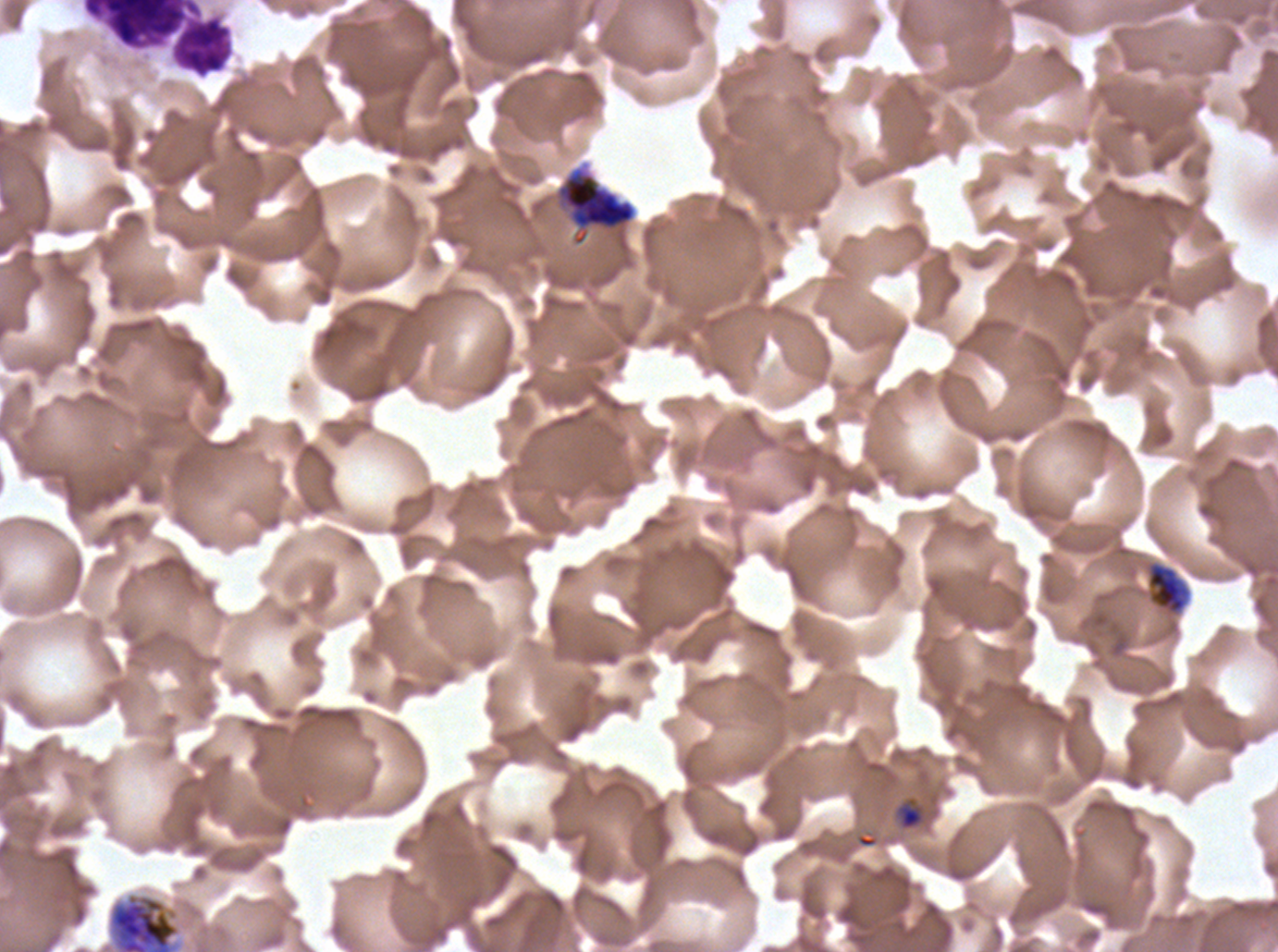

Approximate bounding boxes as {x1, y1, x2, y2} in pixels.
Summary:
  - Mid trophozoite locations: {1146, 561, 1190, 615}
  - Early schizont locations: {557, 167, 636, 246}, {99, 891, 186, 951}
  - Late-ring/early-trophozoite locations: {895, 797, 926, 831}
  - Leukocyte locations: {81, 0, 233, 79}
  - Stain: Giemsa
  - Image size: 1278×952 pixels
  - Field of view: sub-image separated from a larger composite
  - Specimen: P. falciparum cultured ex vivo for 24 to 48 hours, from a patient in The Gambia
  - Life-cycle stages observed: late-ring/early-trophozoite, mid trophozoite, early schizont
  - Preparation: thin blood smear